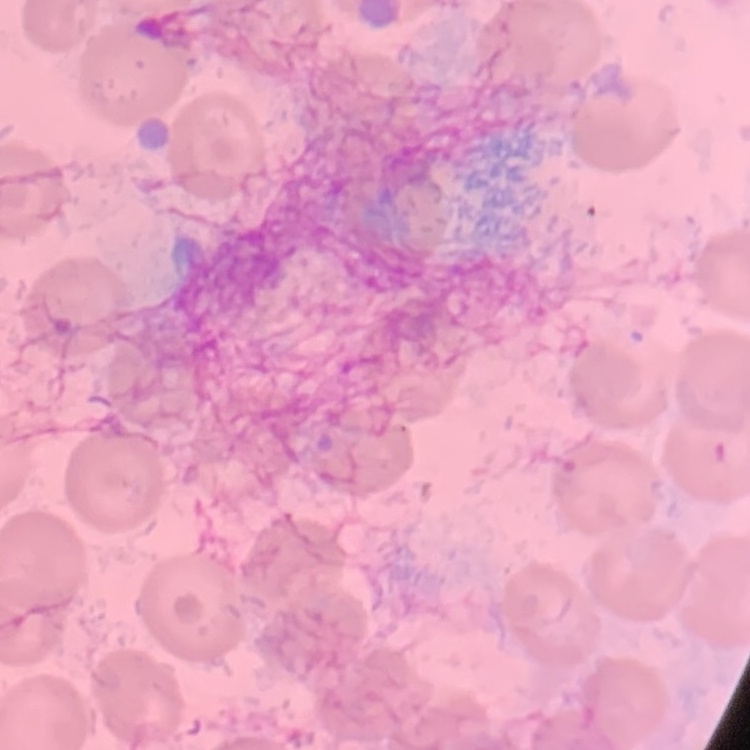 The erythrocytes exhibit no rouleaux formation. Thin peripheral smear. Stained with either Field's or Giemsa. Square crop of a larger photomicrograph.